Locate every blood parasite and identify its species.
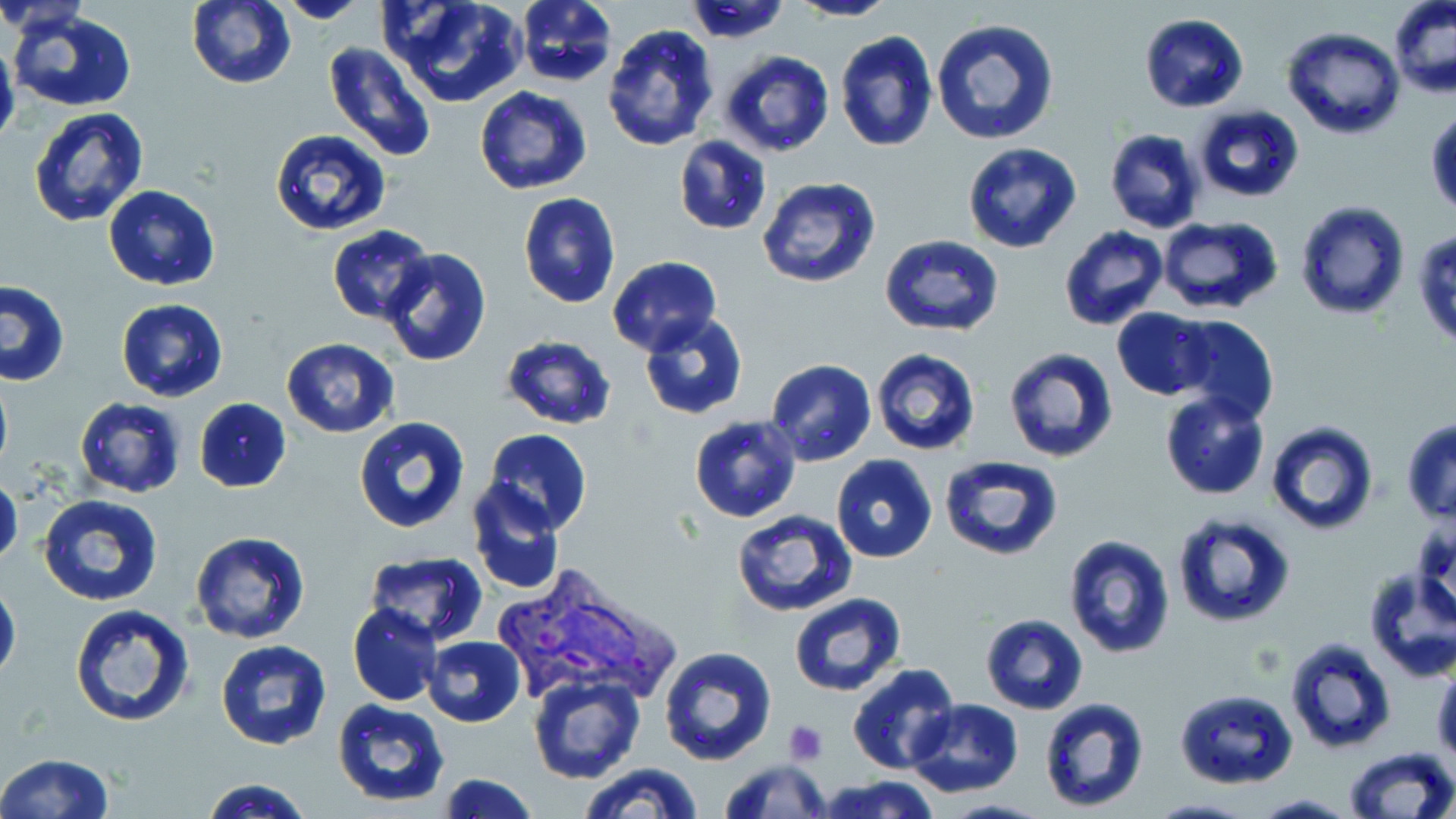
Approximate bounding boxes as [x1, y1, x2, y2] in pixels.
Plasmodium vivax-infected red blood cells: [487, 568, 678, 702].
No Plasmodium falciparum, Plasmodium ovale, Plasmodium malariae, Babesia divergens, or Trypanosoma brucei observed.

Platelet locations: [782, 720, 828, 765]. Uninfected red blood cell locations: [187, 0, 295, 89], [384, 0, 525, 108], [513, 0, 618, 89], [789, 0, 896, 22], [1389, 0, 1455, 98], [276, 1, 368, 24], [0, 3, 91, 37], [6, 7, 138, 112], [1140, 12, 1249, 112], [930, 15, 1059, 146], [601, 24, 718, 151], [1281, 27, 1405, 140], [834, 30, 938, 152], [0, 37, 19, 155], [323, 42, 437, 163], [718, 51, 836, 159], [474, 87, 593, 196], [1193, 104, 1304, 201], [27, 106, 149, 228], [1426, 107, 1456, 217], [1104, 128, 1205, 234], [270, 130, 391, 237], [673, 136, 772, 235], [962, 142, 1082, 254], [757, 177, 882, 290], [103, 185, 221, 290], [518, 193, 621, 309], [1297, 201, 1410, 319], [1155, 216, 1284, 314], [328, 225, 437, 325], [1059, 225, 1168, 331], [1414, 225, 1456, 350], [880, 235, 1004, 337], [380, 247, 491, 366], [607, 256, 722, 356], [0, 281, 70, 386], [116, 298, 228, 402], [1113, 307, 1215, 400], [638, 312, 749, 421], [1171, 315, 1278, 426], [499, 335, 617, 431], [280, 340, 400, 437], [1003, 346, 1121, 464], [870, 348, 983, 456], [765, 358, 877, 465], [0, 369, 13, 482], [1159, 391, 1270, 500], [193, 396, 291, 491], [74, 398, 186, 497], [689, 415, 802, 524], [352, 417, 470, 535], [1401, 419, 1456, 523], [1266, 422, 1377, 534], [483, 429, 594, 535], [831, 454, 938, 563], [939, 455, 1062, 563], [0, 472, 23, 572], [468, 478, 566, 594], [38, 495, 162, 605], [730, 510, 857, 618], [1170, 511, 1295, 628], [190, 530, 308, 643], [1062, 535, 1177, 659], [363, 552, 488, 644], [1361, 566, 1456, 681], [0, 577, 21, 686], [789, 592, 906, 695], [70, 603, 195, 726], [348, 604, 442, 705], [981, 614, 1088, 713], [424, 635, 526, 727], [1285, 636, 1395, 754], [215, 639, 334, 751], [659, 647, 779, 766], [1432, 660, 1455, 766], [846, 663, 961, 777], [528, 673, 646, 786], [1174, 689, 1299, 789], [1038, 697, 1149, 812], [905, 698, 1024, 797], [331, 699, 451, 806], [1342, 746, 1455, 819], [0, 753, 116, 819], [719, 757, 830, 818], [578, 763, 703, 819], [436, 774, 539, 818], [814, 774, 941, 819], [199, 778, 312, 818], [1252, 794, 1357, 817], [1147, 798, 1254, 818]. Slide-level diagnosis: Plasmodium vivax. May-Grünwald-Giemsa stain. 1000x magnification. Image is 1456×819 pixels. Thin blood smear. Light microscopy. Single field of view.